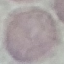
Result: negative for malaria parasites. Acquired by smartphone through the microscope eyepiece. Giemsa-stained preparation. Thin blood smear. Automatically extracted cell patch, resized to 64 × 64 pixels.